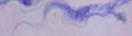
Captured at 1000x magnification. A trypanosome is seen. Micrograph.